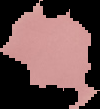

image size = 100×109 pixels
preparation = thin blood film
image type = segmented cell region on a black background
result = no malaria parasites detected